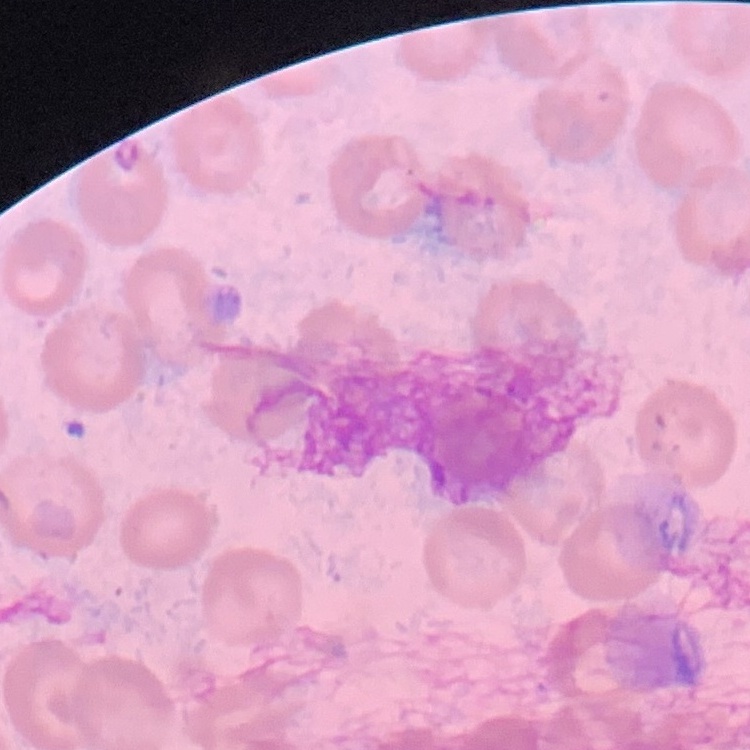
The red blood cells exhibit no rouleaux formation. One tile cut from a larger photomicrograph. Thin peripheral smear. Stained with either Field's or Giemsa.